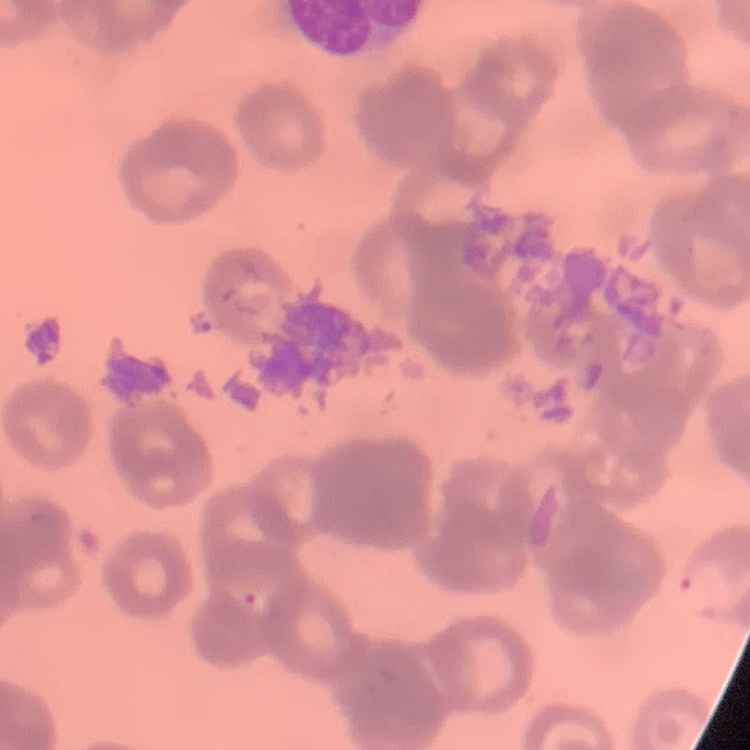

Summary:
  - Red blood cell morphology: rouleaux formation
  - Stain: Field's or Giemsa
  - Image type: square crop of a larger photomicrograph
  - Preparation: thin peripheral smear